Locate every leukocyte (white blood cell).
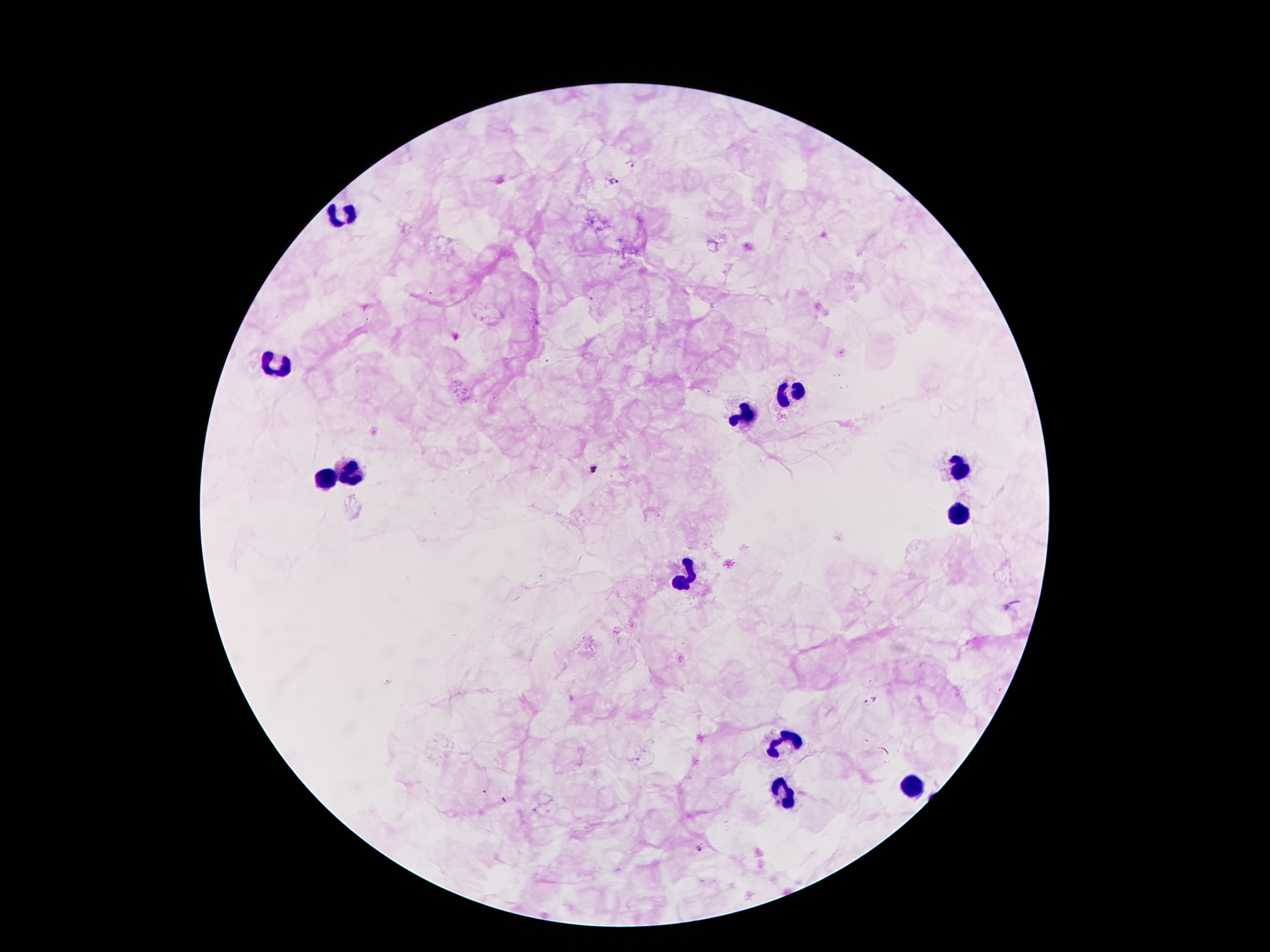

Approximate centers as (x, y) in pixels.
Leukocytes: (344, 214), (279, 365), (790, 393), (747, 417), (960, 470), (348, 473), (324, 478), (956, 513), (687, 574), (785, 742), (910, 783), (785, 795).

Summary:
  - Malaria parasite locations: (632, 163), (613, 179), (594, 469), (870, 701), (699, 848)
  - Field of view: one from this slide
  - Patient malaria status: positive for Plasmodium falciparum
  - Magnification: 100x
  - Stain: Giemsa
  - Capture: smartphone camera through the microscope eyepiece
  - Image size: 1270×952 pixels
  - Preparation: thick blood smear